Report the malaria status.
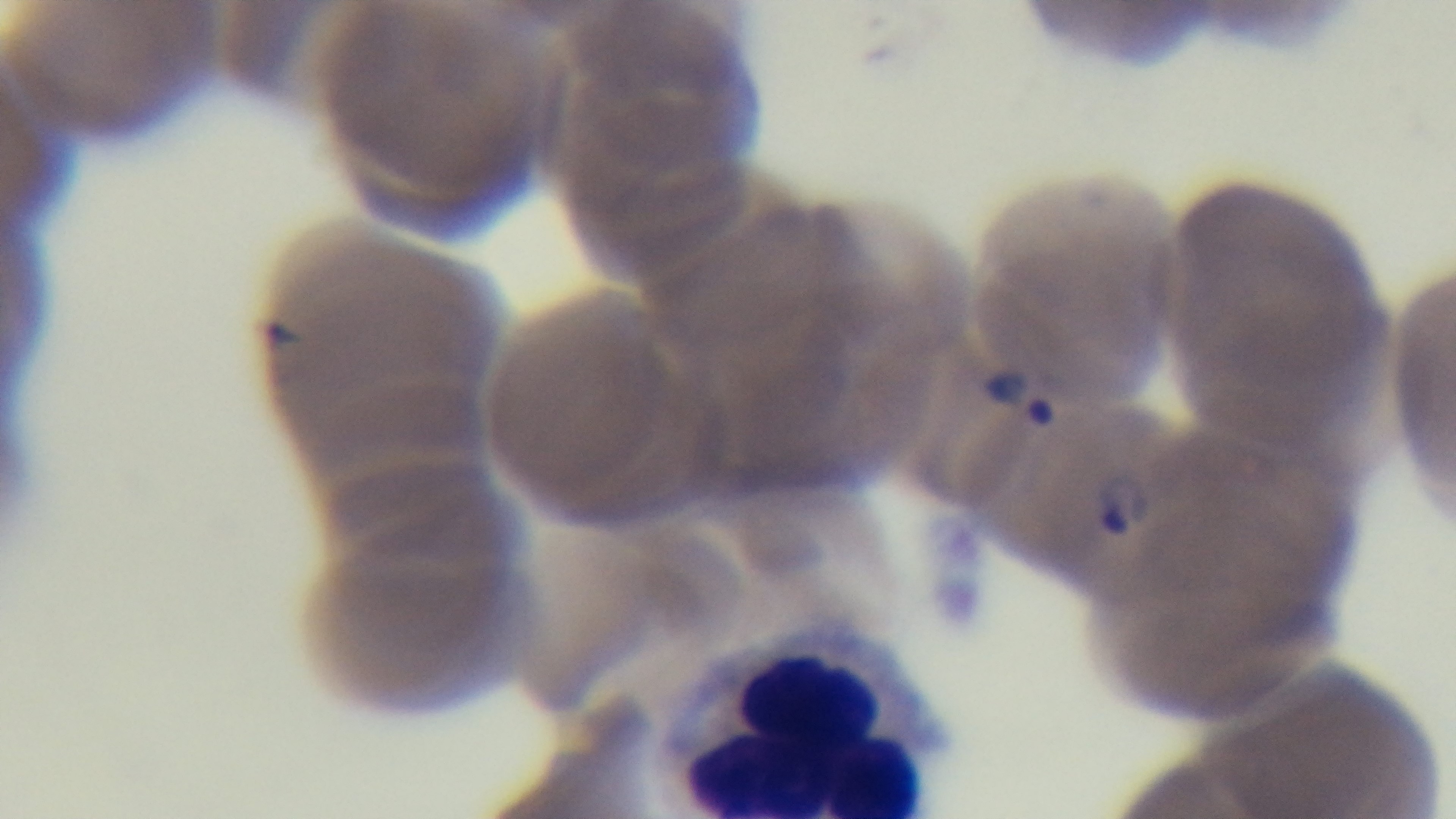

It is infected.

capture: mounted 4K digital camera
objective: 100x oil immersion
modality: light microscopy
preparation: thin smear
stain: Giemsa
field_of_view: one from the slide